Locate and identify every blood parasite.
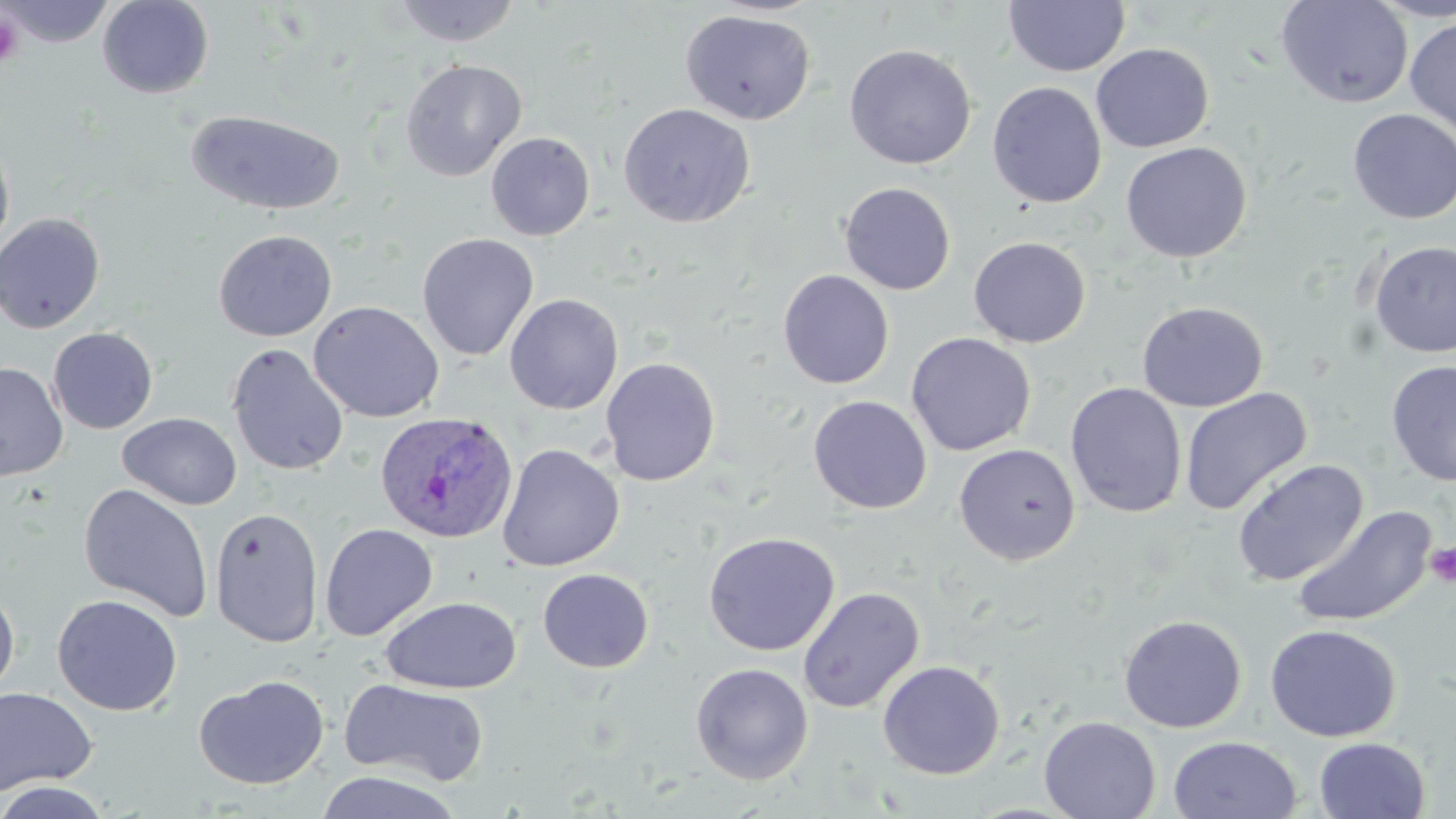

Approximate bounding boxes as (x1,y1)-(x2,y2) corner pairs in pixels.
Plasmodium ovale-infected red blood cells: (374,411)-(519,545).
No Plasmodium falciparum, Plasmodium malariae, Plasmodium vivax, Babesia divergens, or Trypanosoma brucei observed.

slide-level diagnosis = Plasmodium ovale
platelet locations = approximate bounding boxes as (x1,y1)-(x2,y2) corner pairs in pixels: (0,12)-(25,69), (1425,541)-(1456,587)
uninfected red blood cell locations = approximate bounding boxes as (x1,y1)-(x2,y2) corner pairs in pixels: (2,0)-(114,47), (97,0)-(214,99), (391,0)-(522,47), (1275,0)-(1413,109), (1369,0)-(1456,22), (1003,1)-(1130,77), (680,9)-(816,125), (1404,16)-(1456,137), (1091,43)-(1214,152), (843,44)-(977,170), (400,58)-(527,181), (987,81)-(1106,209), (618,102)-(756,228), (1347,108)-(1456,225), (186,109)-(346,216), (486,132)-(596,241), (0,138)-(15,260), (1120,142)-(1252,263), (839,182)-(956,295), (0,212)-(105,334), (213,229)-(337,341), (417,232)-(538,361), (968,236)-(1091,348), (1368,240)-(1456,358), (777,269)-(894,389), (504,293)-(623,414), (308,300)-(445,423), (1136,301)-(1268,412), (48,327)-(158,434), (906,332)-(1036,456), (226,343)-(348,477), (600,356)-(721,487), (1385,360)-(1456,487), (0,361)-(68,482), (1065,382)-(1186,518), (1178,388)-(1311,516), (808,395)-(932,514), (118,412)-(242,510), (497,443)-(625,572), (954,443)-(1081,565), (1231,459)-(1368,587), (77,483)-(214,622), (1292,505)-(1437,629), (209,506)-(325,647), (319,522)-(438,641), (702,531)-(840,656), (537,568)-(654,673), (0,583)-(20,699), (797,587)-(925,714), (52,594)-(183,716), (380,596)-(522,694), (1119,614)-(1247,733), (1264,624)-(1401,742), (877,660)-(1005,779), (690,663)-(813,785), (193,674)-(330,790), (340,677)-(490,786), (0,686)-(98,797), (1038,715)-(1161,819), (1167,735)-(1302,819), (1313,736)-(1430,818), (313,770)-(466,818), (0,780)-(115,819)
magnification = 1000x
image size = 1456×819 pixels
modality = light microscopy
field of view = one of a larger specimen
preparation = thin blood smear
stain = May-Grünwald-Giemsa